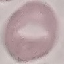
result = negative for malaria parasites
capture = smartphone through the microscope eyepiece
stain = Giemsa
image type = automatically extracted cell patch, resized to 64 × 64 pixels
preparation = thin smear